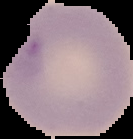

image size = 133×139 pixels
preparation = thin blood smear
malaria status = uninfected
image type = segmented cell region with the area outside set to black